Classify this cell by malaria status.
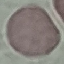

It is uninfected.

Summary:
  - Stain: Giemsa
  - Image type: automatically extracted cell patch, resized to 64 × 64 pixels
  - Capture: smartphone through the microscope eyepiece
  - Preparation: thin blood smear